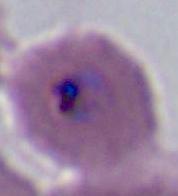

Summary:
  - Magnification: 400x or 1000x
  - Modality: micrograph
  - Identification: Plasmodium